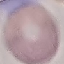 Malaria status: uninfected. Thin smear of blood. Automatically extracted cell patch, resized to 64 × 64 pixels. Acquired by smartphone through the microscope eyepiece. Giemsa-stained preparation.